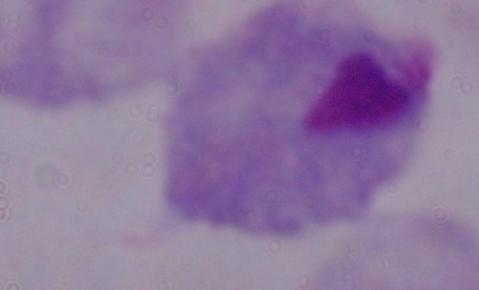
Summary:
  - Identification: trichomonad
  - Magnification: 1000x
  - Modality: photomicrograph